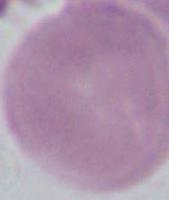
magnification = 1000x
identification = erythrocyte
modality = photomicrograph